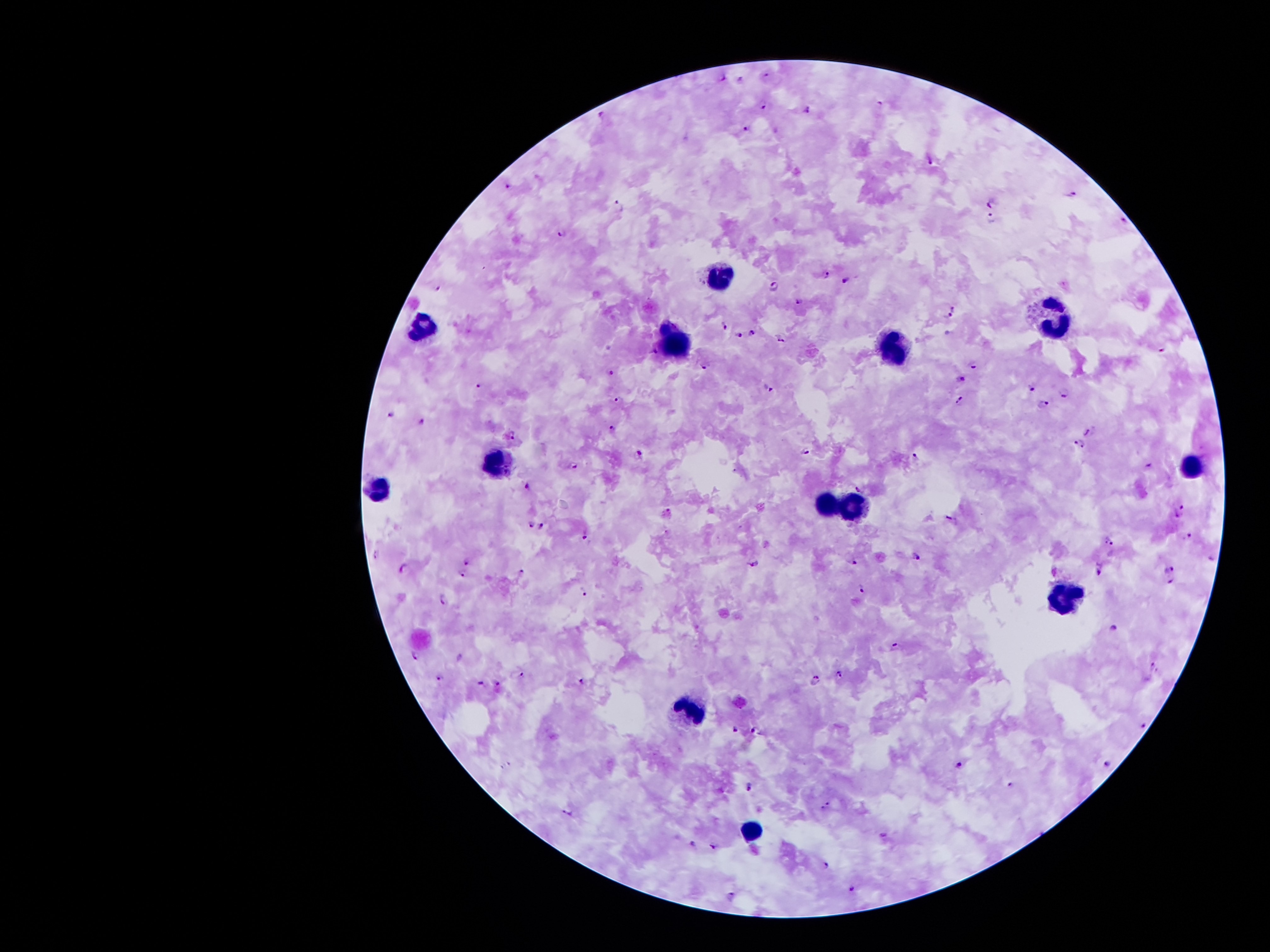

coordinate format = approximate object centers, in pixels from the top-left corner
leukocyte locations = (x=719, y=277), (x=1054, y=320), (x=421, y=325), (x=670, y=335), (x=893, y=354), (x=491, y=461), (x=1194, y=464), (x=378, y=485), (x=822, y=500), (x=855, y=510), (x=1068, y=598), (x=691, y=708), (x=750, y=830)
Plasmodium parasite locations = (x=723, y=79), (x=740, y=79), (x=761, y=103), (x=881, y=103), (x=807, y=109), (x=600, y=116), (x=749, y=129), (x=931, y=160), (x=509, y=183), (x=1073, y=196), (x=991, y=202), (x=620, y=207), (x=1123, y=216), (x=992, y=220), (x=562, y=233), (x=825, y=276), (x=846, y=281), (x=774, y=285), (x=438, y=287), (x=798, y=301), (x=953, y=309), (x=947, y=318), (x=723, y=327), (x=752, y=331), (x=738, y=336), (x=781, y=337), (x=1162, y=350), (x=652, y=351), (x=706, y=365), (x=973, y=365), (x=611, y=371), (x=960, y=377), (x=480, y=385), (x=769, y=388), (x=1031, y=388), (x=1065, y=392), (x=619, y=399), (x=959, y=401), (x=1041, y=407), (x=390, y=415), (x=423, y=419), (x=611, y=427), (x=1090, y=431), (x=512, y=434), (x=1078, y=443), (x=806, y=451), (x=637, y=452), (x=917, y=456), (x=574, y=466), (x=1149, y=466), (x=526, y=486), (x=859, y=488), (x=1183, y=507), (x=668, y=511), (x=1178, y=516), (x=953, y=521), (x=530, y=525), (x=542, y=526), (x=584, y=534), (x=1189, y=537), (x=1110, y=541), (x=375, y=554), (x=917, y=556), (x=849, y=559), (x=1212, y=559), (x=753, y=563), (x=468, y=564), (x=1170, y=568), (x=1100, y=569), (x=404, y=570), (x=522, y=572), (x=463, y=574), (x=1171, y=583), (x=862, y=588), (x=582, y=590), (x=443, y=600), (x=1112, y=627), (x=896, y=647), (x=416, y=656), (x=1155, y=667), (x=838, y=673), (x=522, y=674), (x=440, y=677), (x=814, y=681), (x=481, y=682), (x=581, y=682), (x=498, y=683), (x=1144, y=726), (x=736, y=728), (x=757, y=729), (x=960, y=765), (x=1109, y=765), (x=1011, y=784), (x=751, y=785), (x=826, y=806), (x=568, y=812), (x=882, y=834), (x=694, y=843), (x=713, y=844), (x=827, y=866), (x=851, y=890), (x=732, y=896)
image size = 1270×952 pixels
magnification = 100x
capture = smartphone camera through the microscope eyepiece
patient malaria status = positive for Plasmodium falciparum
preparation = thick blood film
stain = Giemsa
field of view = one from this slide